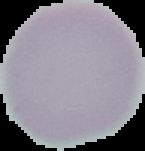
image type = cell region segmented out of the field of view; surrounding area masked to black
preparation = thin blood smear
result = no Plasmodium parasites seen
image size = 145×151 pixels